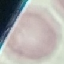
result = no malaria parasites seen
image type = cell patch, automatically extracted from a larger field of view and resized to 64 × 64 pixels
preparation = thin blood smear
capture = smartphone camera at the microscope eyepiece
stain = Giemsa